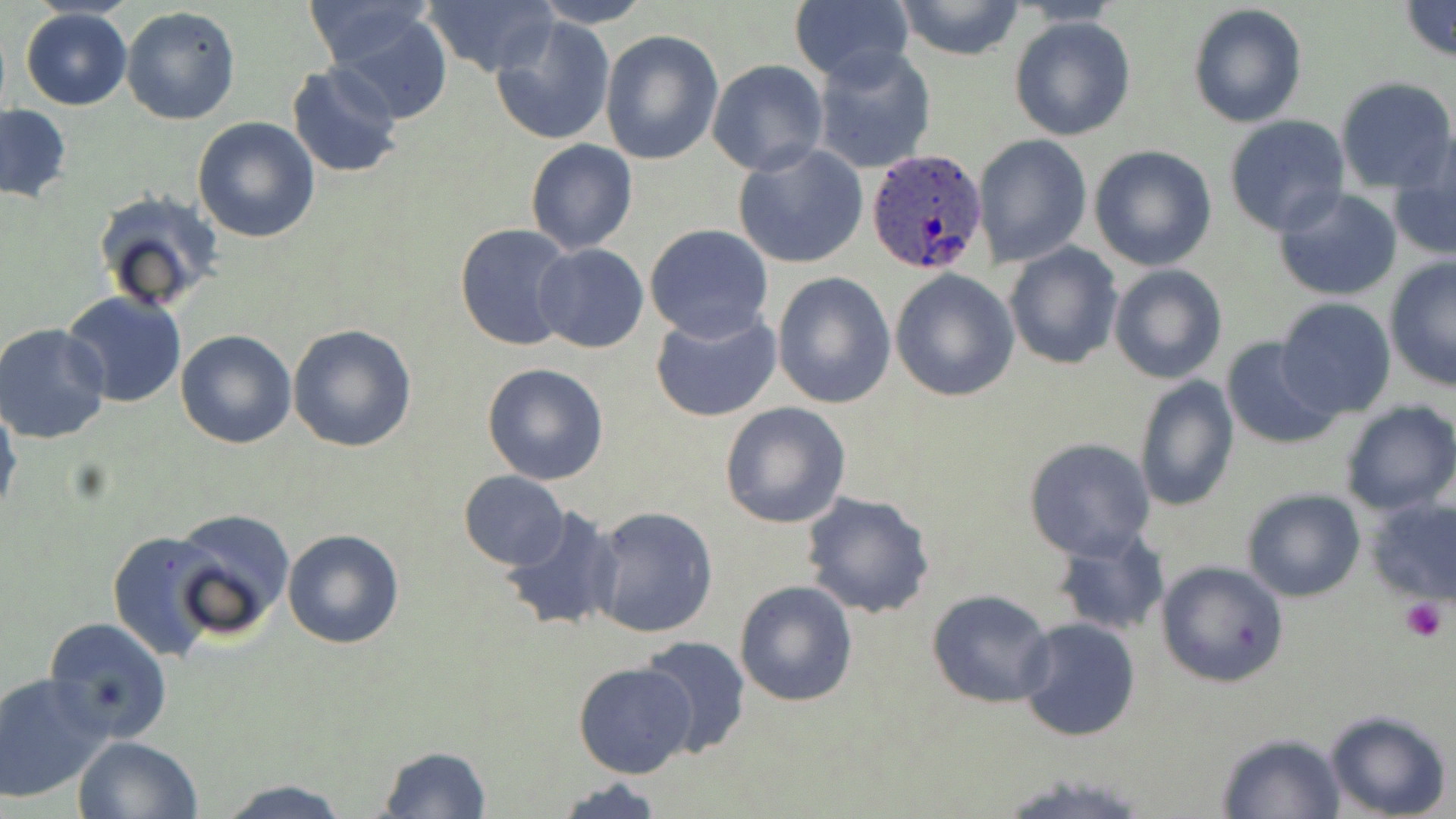
Approximate bounding boxes as (x1,y1)-(x2,y2) corner pairs in pixels. Uninfected red blood cell locations: (424,0)-(558,75), (531,0)-(654,28), (893,0)-(1026,61), (301,2)-(441,73), (787,2)-(913,85), (1398,2)-(1456,62), (1187,4)-(1309,129), (119,6)-(241,126), (21,8)-(131,109), (325,8)-(455,124), (487,12)-(618,145), (1008,16)-(1136,141), (600,29)-(724,164), (810,44)-(936,175), (706,58)-(829,177), (286,61)-(405,177), (1334,77)-(1455,193), (0,104)-(70,201), (1223,116)-(1351,236), (193,117)-(321,243), (1389,132)-(1456,263), (972,134)-(1092,265), (525,140)-(637,254), (733,144)-(869,269), (1088,145)-(1218,271), (1272,188)-(1404,300), (92,190)-(225,315), (455,223)-(579,353), (644,224)-(774,342), (1003,241)-(1123,370), (532,243)-(651,353), (1383,258)-(1456,393), (1109,264)-(1227,385), (889,267)-(1021,402), (771,271)-(896,410), (62,290)-(189,409), (1274,298)-(1397,420), (650,305)-(783,424), (1,322)-(114,446), (287,323)-(417,451), (176,328)-(297,450), (1222,336)-(1344,449), (481,362)-(610,485), (1134,376)-(1240,511), (1338,401)-(1456,517), (0,402)-(23,526), (719,402)-(852,529), (1022,437)-(1155,561), (458,472)-(568,571), (798,489)-(936,620), (1242,489)-(1365,603), (1363,494)-(1456,603), (586,505)-(720,640), (501,506)-(622,635), (173,508)-(295,638), (280,528)-(405,649), (1053,528)-(1170,638), (108,529)-(230,661), (1155,560)-(1289,687), (734,579)-(858,704), (926,590)-(1056,709), (43,616)-(174,746), (1016,616)-(1141,742), (638,636)-(751,758), (573,660)-(697,779), (1,672)-(110,803), (1323,709)-(1452,819), (1216,732)-(1348,818), (72,735)-(201,819), (375,746)-(492,818), (212,778)-(353,817), (552,778)-(668,818). Plasmodium ovale-infected red blood cell locations: (866,147)-(991,275). Platelet locations: (1400,598)-(1450,642). Slide-level diagnosis: Plasmodium ovale. Single field of view. Thin blood smear. Captured at 1000x magnification. Image is 1456×819 pixels. May-Grünwald-Giemsa-stained preparation. Optical microscopy.